Comment on the morphology of the erythrocytes.
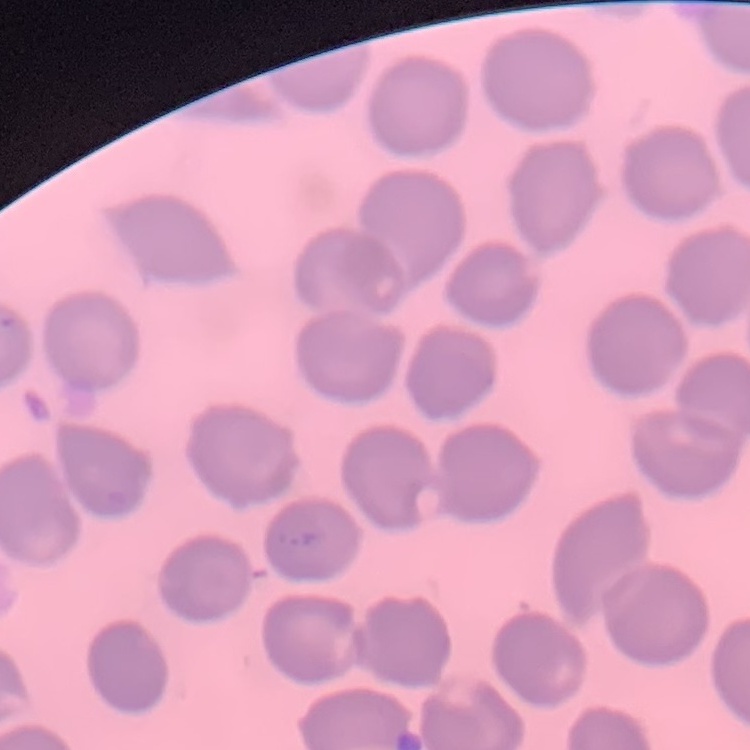

No rouleaux formation.

Summary:
  - Image type: square crop of a larger photomicrograph
  - Preparation: thin blood smear
  - Stain: Field's or Giemsa